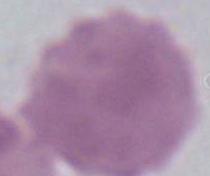

Micrograph. An erythrocyte is shown. 1000x magnification.